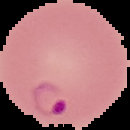

Summary:
  - Malaria status: parasitized
  - Image size: 130×130 pixels
  - Preparation: thin blood smear
  - Image type: segmented cell region with the area outside set to black